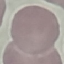 Result: no malaria parasites seen. Photographed with a smartphone camera at the microscope eyepiece. Giemsa-stained preparation. Thin blood film. Cell patch, automatically extracted from a larger field of view and resized to 64 × 64 pixels.